Assess this cell for malaria.
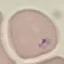
Parasitized.

Giemsa stain. Automatically extracted cell patch, resized to 64 × 64 pixels. Thin blood smear. Photographed with a smartphone camera at the microscope eyepiece.